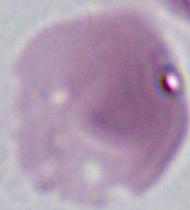

Photomicrograph. 1000x magnification. A red blood cell is seen.